Assess this cell for malaria.
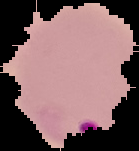

Parasitized.

Image is 139×151 pixels. The area outside the segmented cell region is set to black. From a thin blood film.